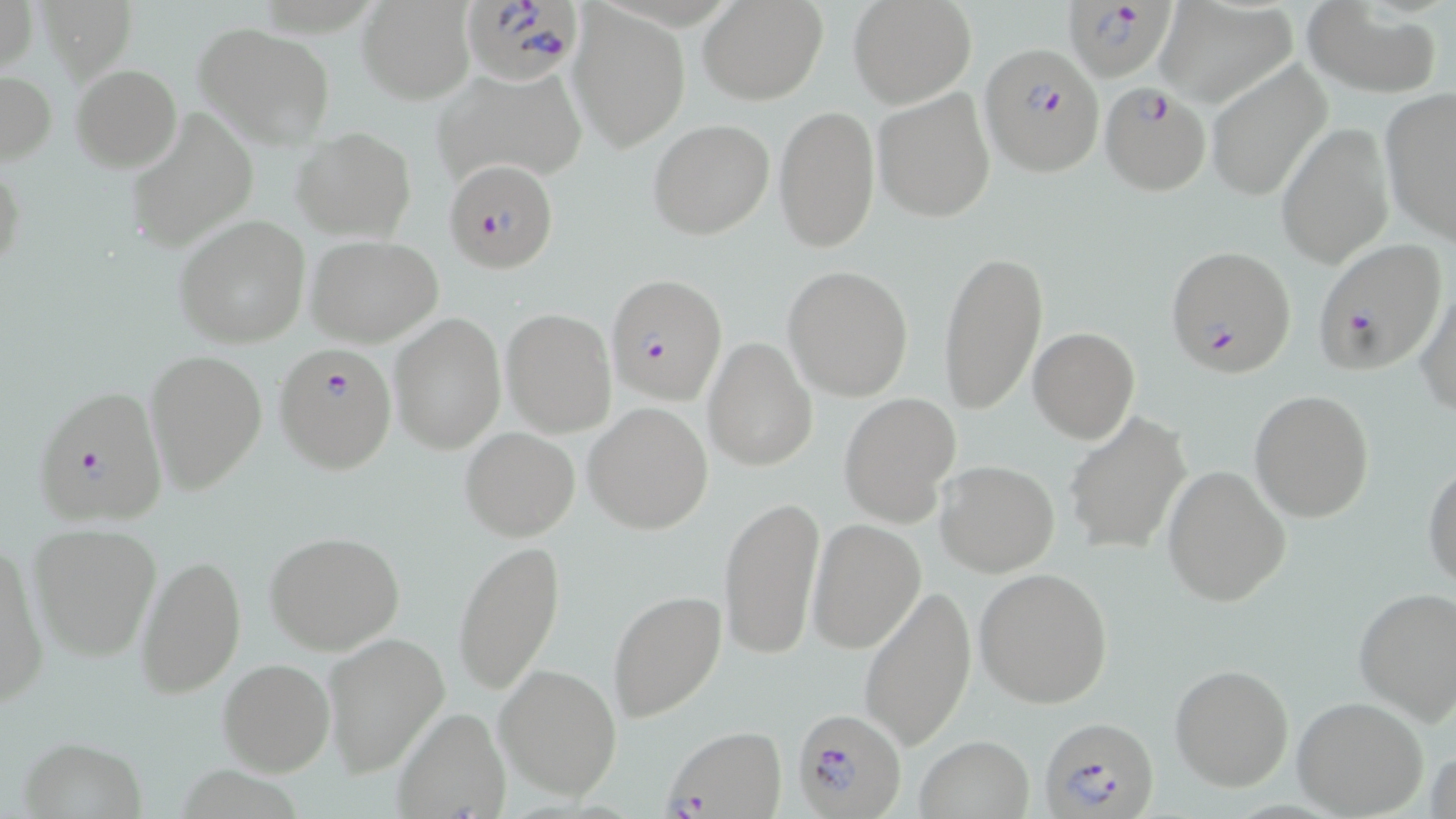

slide_level_diagnosis: Plasmodium falciparum
magnification: 1000x
uninfected_red_blood_cell_locations: 'approximate bounding boxes as (x1,y1)-(x2,y2) corner pairs in pixels: (1,0)-(37,78), (699,0)-(827,105), (849,0)-(977,108), (1156,1)-(1297,108), (358,3)-(474,104), (1303,3)-(1441,97), (569,7)-(691,151), (194,22)-(336,149), (1203,59)-(1332,204), (71,65)-(181,170), (431,65)-(590,190), (0,69)-(56,166), (872,87)-(997,224), (1379,89)-(1456,243), (773,104)-(880,254), (125,106)-(258,255), (648,119)-(775,240), (1276,121)-(1396,270), (291,128)-(417,241), (0,154)-(26,282), (173,215)-(311,348), (308,236)-(443,348), (938,246)-(1048,417), (782,264)-(914,401), (1416,278)-(1456,418), (501,308)-(617,437), (388,313)-(507,455), (1028,327)-(1138,442), (703,336)-(817,472), (143,348)-(267,493), (1249,389)-(1375,522), (838,394)-(959,525), (584,402)-(713,535), (1064,411)-(1191,554), (460,427)-(579,541), (935,460)-(1059,577), (1424,462)-(1456,591), (1162,465)-(1292,606), (719,494)-(826,661), (808,520)-(924,653), (26,521)-(163,662), (263,531)-(408,656), (452,538)-(566,694), (1,540)-(50,710), (136,550)-(246,696), (974,567)-(1113,709), (858,584)-(977,751), (1353,586)-(1456,726), (607,588)-(726,724), (320,631)-(451,777), (217,657)-(335,777), (494,661)-(622,801), (1169,663)-(1294,791), (1292,696)-(1429,817), (393,708)-(510,817), (17,734)-(149,818), (914,736)-(1036,818), (1426,745)-(1456,819)'
plasmodium_falciparum_infected_red_blood_cell_locations: 'approximate bounding boxes as (x1,y1)-(x2,y2) corner pairs in pixels: (459,0)-(583,87), (1065,0)-(1178,80), (980,43)-(1102,175), (1099,81)-(1214,195), (444,159)-(559,274), (1312,239)-(1446,376), (1165,244)-(1297,378), (608,273)-(725,406), (275,344)-(398,473), (32,386)-(170,527), (791,708)-(906,817), (1040,715)-(1159,819), (661,726)-(786,818)'
image_size: 1456×819 pixels
preparation: thin blood film
field_of_view: single
modality: optical microscopy
stain: May-Grünwald-Giemsa